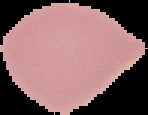

Summary:
  - Image type: segmented cell region with the area outside set to black
  - Preparation: thin blood film
  - Result: no Plasmodium parasites detected
  - Image size: 148×115 pixels